Point out each leukocyte.
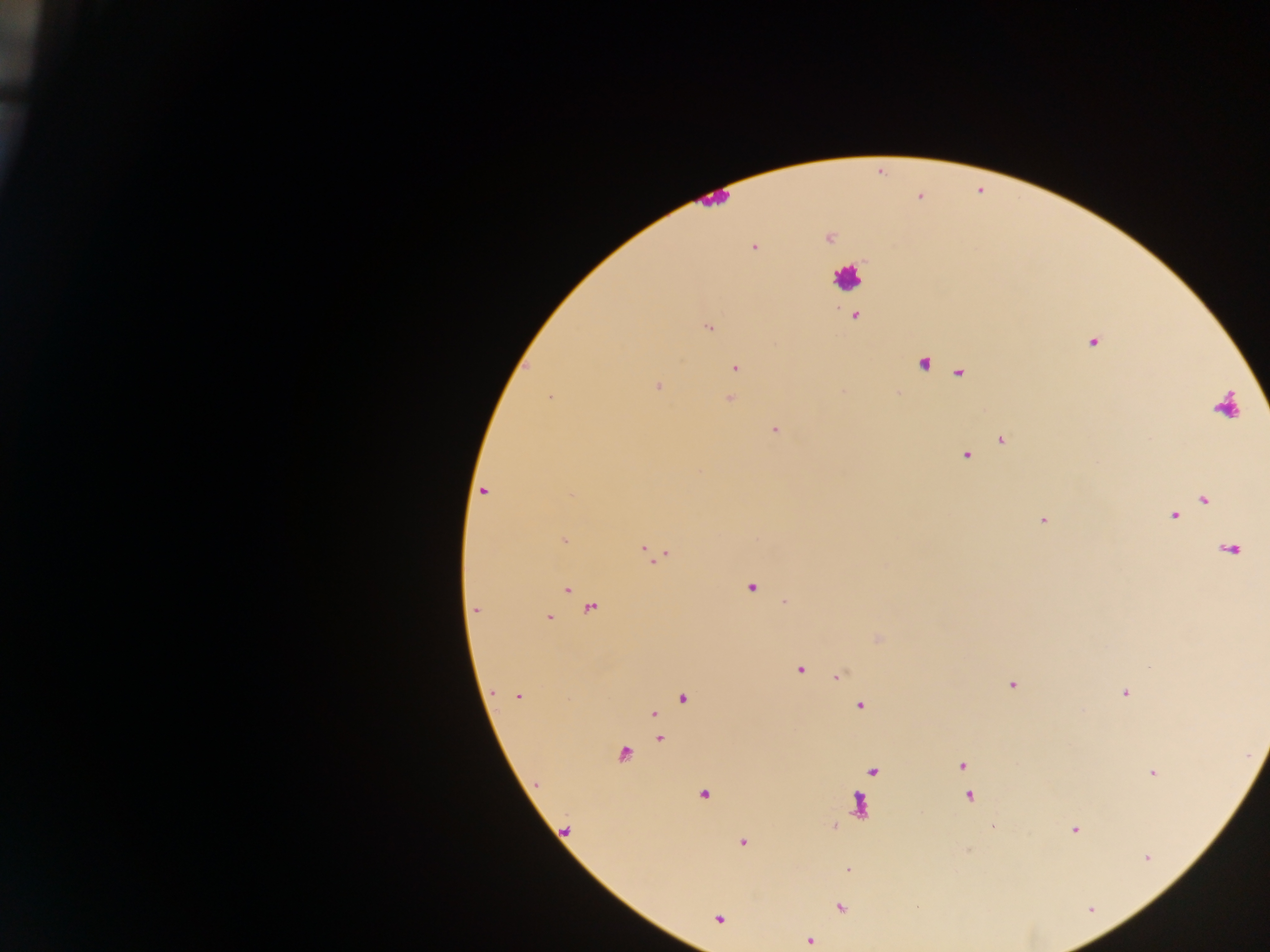

Approximate centers as x y in pixels.
Leukocytes: 847 278.

Malaria parasite locations: 828 238; 754 246; 855 316; 708 327; 1093 342; 923 364; 735 368; 658 386; 549 397; 730 399; 775 430; 1001 440; 965 456; 484 491; 1204 500; 1174 516; 1043 520; 564 540; 649 551; 658 555; 750 587; 567 589; 591 609; 475 611; 549 618; 800 670; 838 675; 1012 684; 1125 693; 518 697; 682 698; 859 706; 654 714; 659 738; 623 755; 962 766; 1153 773; 704 794; 970 797; 834 826; 1075 830; 743 842; 1147 857; 849 869; 840 907; 719 918; 809 941. Single field of view. Thick blood film. Image is 1270×952 pixels. Mobile-phone photograph taken through the microscope. Collected in Ghana.